Comment on the morphology of the erythrocytes.
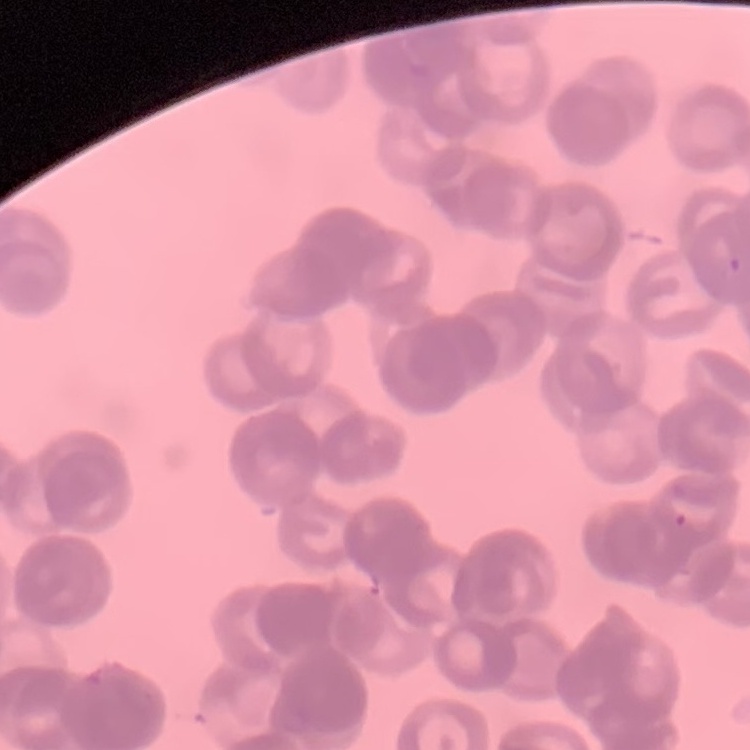
They show rouleaux formation.

Summary:
  - Preparation: thin peripheral smear
  - Stain: Field's or Giemsa
  - Image type: square crop of a larger photomicrograph